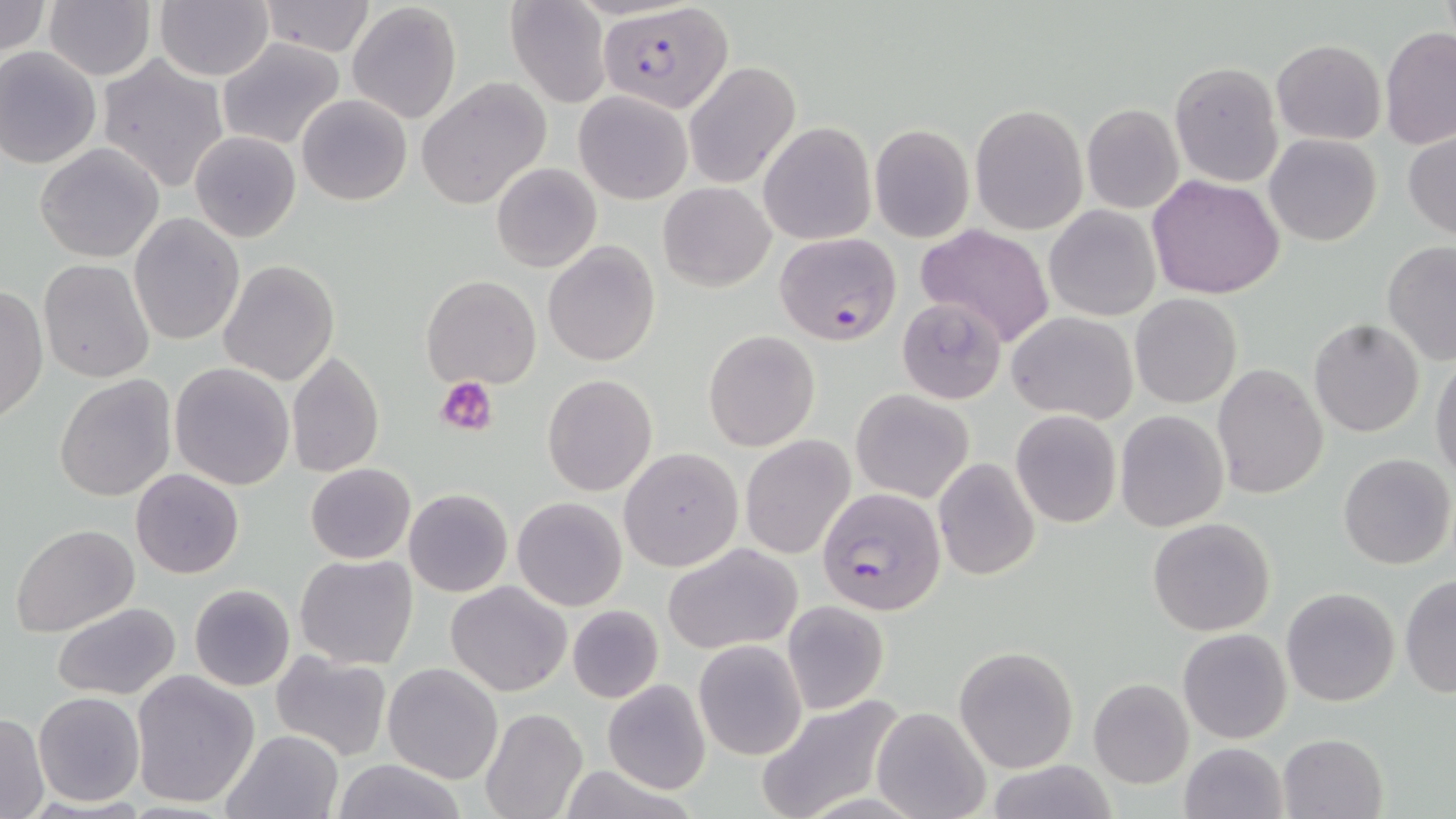

plasmodium_falciparum_infected_red_blood_cell_locations: 'approximate bounding boxes as [x1, y1, x2, y2] in pixels: [599, 2, 732, 112], [774, 232, 902, 347], [816, 486, 946, 614]'
slide_level_diagnosis: Plasmodium falciparum
stain: May-Grünwald-Giemsa
modality: light microscopy
uninfected_red_blood_cell_locations: 'approximate bounding boxes as [x1, y1, x2, y2] in pixels: [44, 0, 156, 81], [154, 0, 274, 81], [505, 0, 611, 108], [0, 1, 50, 59], [259, 1, 378, 57], [346, 2, 464, 124], [1379, 27, 1456, 151], [217, 38, 344, 149], [1271, 39, 1386, 144], [0, 46, 101, 169], [97, 54, 229, 194], [683, 61, 800, 188], [1170, 62, 1282, 186], [416, 79, 551, 210], [574, 91, 692, 204], [296, 94, 411, 205], [970, 104, 1088, 234], [1082, 104, 1184, 213], [758, 121, 876, 245], [870, 123, 974, 242], [1403, 131, 1456, 239], [189, 132, 300, 243], [1264, 133, 1382, 246], [35, 143, 164, 263], [492, 161, 602, 273], [1147, 175, 1284, 299], [659, 183, 774, 291], [1044, 205, 1161, 321], [129, 215, 244, 345], [917, 224, 1056, 348], [1380, 240, 1455, 366], [543, 241, 660, 367], [39, 259, 156, 384], [220, 260, 339, 386], [423, 274, 540, 388], [0, 285, 48, 424], [1129, 294, 1242, 408], [896, 295, 1006, 403], [1007, 312, 1137, 424], [1308, 318, 1426, 437], [702, 329, 819, 451], [285, 350, 384, 480], [1430, 357, 1456, 485], [169, 362, 295, 489], [1211, 363, 1327, 500], [541, 373, 659, 497], [54, 374, 177, 502], [850, 390, 974, 503], [1010, 410, 1121, 528], [1115, 410, 1229, 531], [740, 436, 855, 558], [618, 447, 743, 571], [1338, 453, 1455, 570], [933, 457, 1041, 583], [304, 463, 415, 564], [130, 468, 244, 579], [404, 488, 513, 597], [512, 496, 627, 611], [1147, 517, 1276, 637], [12, 524, 138, 639], [664, 542, 804, 653], [295, 554, 419, 670], [1400, 576, 1456, 697], [445, 581, 572, 697], [188, 584, 295, 691], [1281, 586, 1400, 707], [781, 601, 889, 715], [52, 602, 183, 701], [567, 604, 663, 703], [1178, 627, 1292, 744], [693, 640, 808, 761], [954, 645, 1077, 773], [270, 651, 393, 761], [383, 663, 502, 784], [131, 670, 261, 810], [1088, 678, 1193, 788], [603, 680, 713, 794], [32, 692, 144, 806], [755, 696, 905, 819], [873, 706, 990, 819], [481, 708, 587, 819], [0, 711, 48, 819], [223, 730, 345, 819], [1277, 732, 1388, 818], [1178, 742, 1287, 819], [331, 758, 466, 819], [981, 760, 1122, 818], [555, 764, 702, 819]'
magnification: 1000x
platelet_locations: 'approximate bounding boxes as [x1, y1, x2, y2] in pixels: [438, 378, 498, 437]'
preparation: thin blood film
field_of_view: one of a larger specimen
image_size: 1456×819 pixels